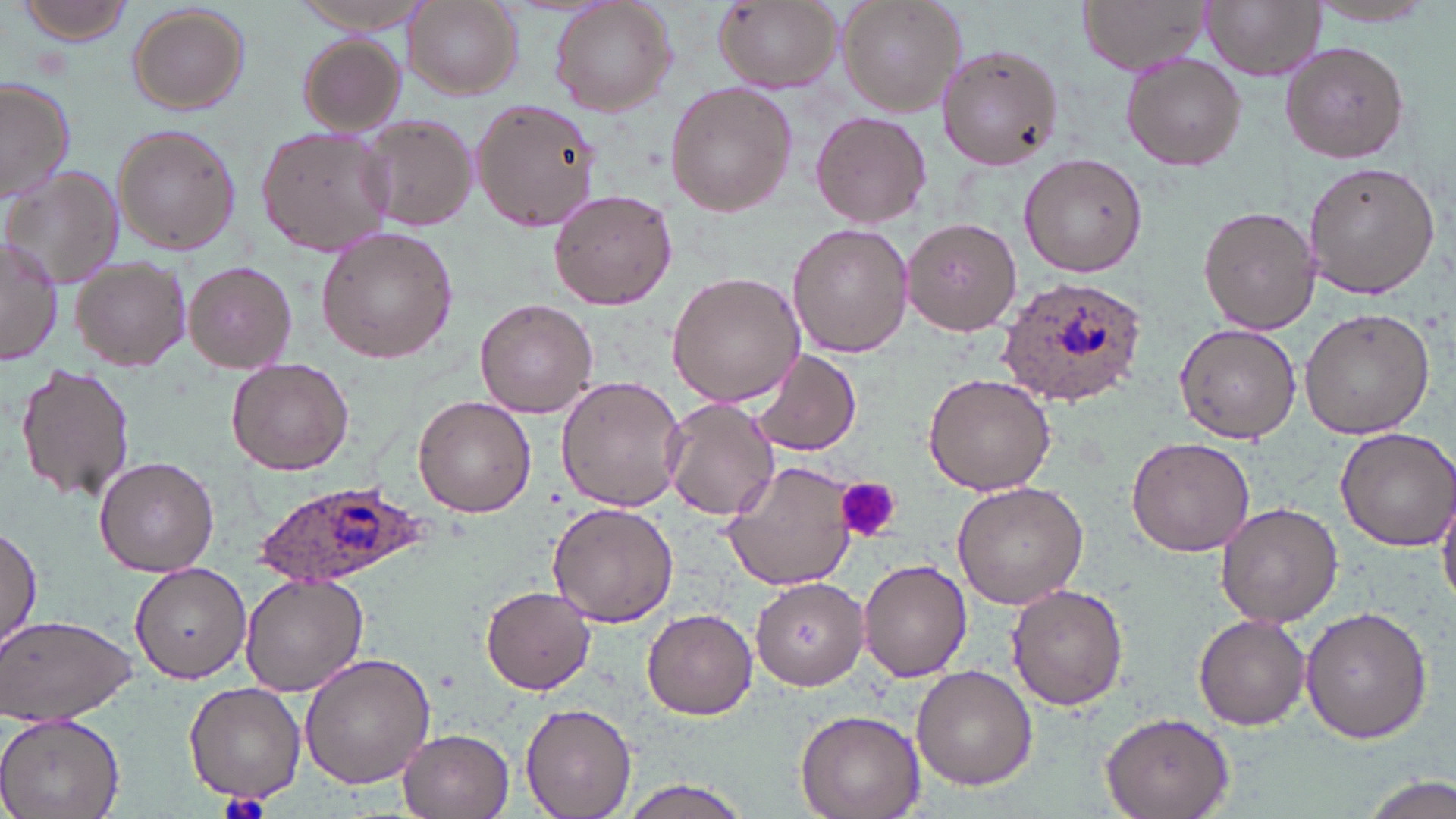

Summary:
  - Coordinate format: approximate bounding boxes as [x1, y1, x2, y2] in pixels
  - Plasmodium ovale-infected red blood cell locations: [999, 277, 1147, 404], [257, 480, 434, 589]
  - Uninfected red blood cell locations: [13, 0, 137, 47], [293, 0, 432, 33], [549, 0, 679, 116], [839, 0, 967, 116], [1075, 0, 1212, 75], [1203, 0, 1322, 82], [402, 1, 522, 99], [1303, 1, 1442, 27], [712, 2, 841, 93], [126, 3, 251, 115], [296, 34, 404, 135], [937, 41, 1065, 172], [1281, 41, 1408, 165], [1122, 54, 1246, 170], [0, 75, 75, 207], [667, 82, 797, 217], [473, 100, 598, 232], [810, 109, 932, 228], [359, 113, 479, 234], [112, 126, 242, 254], [257, 127, 392, 257], [1019, 152, 1148, 277], [1303, 161, 1439, 298], [6, 170, 123, 287], [548, 189, 677, 310], [1198, 208, 1320, 332], [902, 218, 1022, 334], [786, 221, 914, 358], [318, 226, 456, 362], [0, 233, 63, 366], [71, 255, 192, 371], [184, 261, 297, 371], [667, 271, 806, 407], [474, 299, 596, 419], [1301, 308, 1434, 438], [1174, 323, 1300, 444], [752, 349, 862, 457], [226, 358, 354, 475], [16, 362, 136, 505], [923, 373, 1055, 495], [557, 377, 687, 513], [415, 396, 536, 516], [662, 399, 779, 521], [1334, 427, 1456, 551], [1128, 434, 1258, 556], [93, 456, 219, 575], [722, 460, 857, 591], [953, 481, 1089, 608], [1438, 484, 1456, 609], [547, 501, 677, 628], [1215, 501, 1346, 627], [1, 523, 42, 660], [858, 558, 972, 681], [130, 563, 251, 682], [239, 573, 368, 696], [752, 577, 869, 689], [482, 584, 596, 693], [1006, 584, 1129, 712], [1300, 605, 1433, 745], [641, 607, 758, 718], [0, 613, 136, 726], [1193, 613, 1311, 729], [299, 652, 436, 790], [911, 665, 1037, 789], [184, 682, 305, 803], [521, 702, 636, 818], [795, 707, 927, 819], [0, 710, 126, 819], [1100, 711, 1236, 819], [398, 729, 514, 818], [1364, 776, 1452, 819], [618, 777, 754, 819]
  - Platelet locations: [837, 477, 898, 543], [216, 791, 273, 819]
  - Slide-level diagnosis: Plasmodium ovale
  - Stain: May-Grünwald-Giemsa
  - Modality: light microscopy
  - Field of view: single
  - Preparation: thin blood smear
  - Image size: 1456×819 pixels
  - Magnification: 1000x